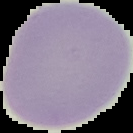

preparation = thin blood film
image type = segmented cell region on a black background
image size = 133×133 pixels
malaria status = uninfected